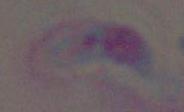

Summary:
  - Magnification: 1000x
  - Modality: photomicrograph
  - Identification: Toxoplasma gondii